Classify this cell by malaria status.
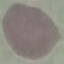

Uninfected.

Summary:
  - Preparation: thin blood film
  - Image type: cell patch, automatically extracted from a larger field of view and resized to 64 × 64 pixels
  - Stain: Giemsa
  - Capture: smartphone through the microscope eyepiece